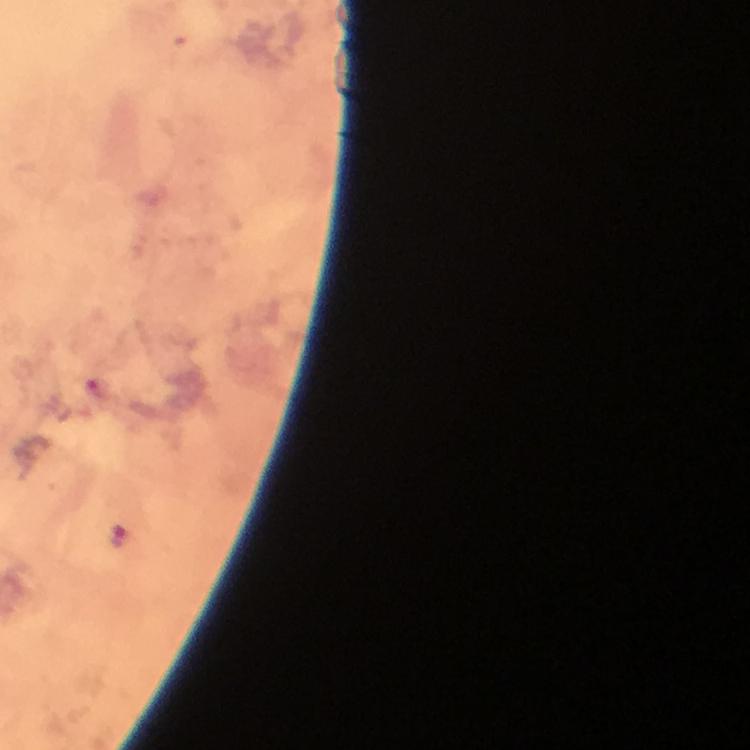

Approximate object centers, in pixels from the top-left corner. Plasmodium parasite locations: (x=120, y=535). Immersion oil was used. Cropped region of a single field of view. From a diagnostic examination for malaria. At 100x magnification. Giemsa stain. Image is 750×750 pixels. Thick smear. Photographed with a smartphone mounted on the microscope.